Name the blood parasite species.
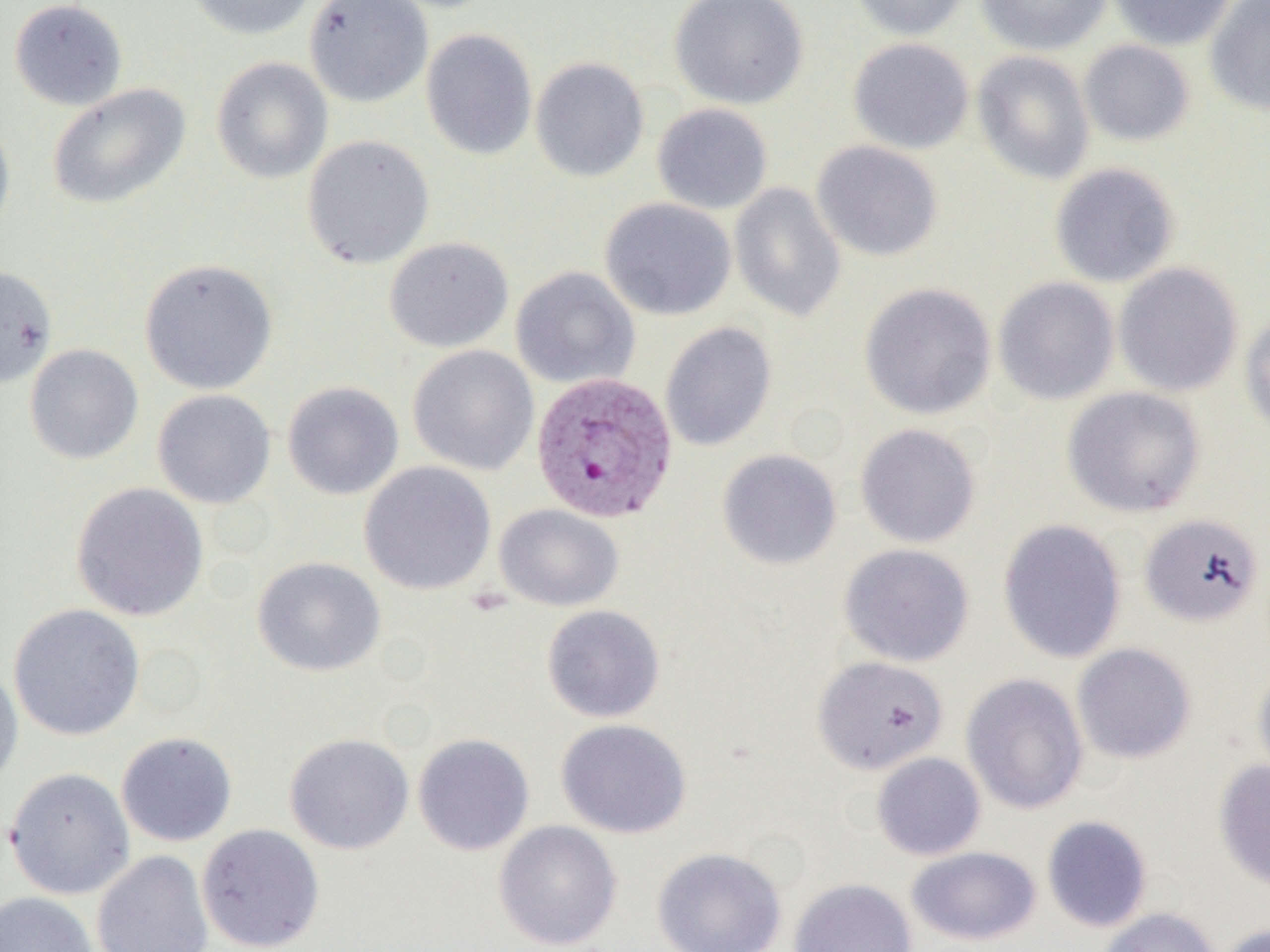

Plasmodium vivax.

Approximate bounding boxes as (x1,y1)-(x2,y2) corner pairs in pixels. Plasmodium vivax-infected red blood cell locations: (529,373)-(676,525). Uninfected red blood cell locations: (8,0)-(128,111), (185,0)-(317,40), (304,0)-(434,107), (669,0)-(810,109), (845,0)-(972,41), (974,0)-(1113,56), (1106,0)-(1239,50), (1205,1)-(1270,116), (421,28)-(538,160), (848,38)-(975,155), (1078,39)-(1195,147), (971,50)-(1095,185), (211,56)-(333,184), (530,57)-(650,182), (47,82)-(191,210), (652,103)-(773,215), (0,114)-(16,246), (301,135)-(435,269), (811,140)-(943,262), (1049,162)-(1180,288), (729,182)-(847,323), (600,197)-(737,320), (383,237)-(514,353), (139,258)-(278,395), (1113,262)-(1243,397), (0,263)-(58,389), (511,267)-(640,389), (993,277)-(1119,405), (859,282)-(997,420), (1239,311)-(1270,437), (660,321)-(777,451), (24,343)-(144,465), (407,344)-(539,475), (282,380)-(404,500), (1062,386)-(1206,518), (152,389)-(276,509), (855,423)-(981,548), (717,448)-(842,570), (359,461)-(496,596), (70,482)-(209,622), (494,503)-(624,611), (1139,513)-(1264,627), (998,519)-(1126,664), (838,543)-(974,667), (252,556)-(386,677), (7,603)-(145,741), (541,604)-(665,723), (1071,643)-(1196,764), (812,656)-(948,775), (0,661)-(24,790), (1252,662)-(1270,789), (961,672)-(1089,814), (556,718)-(691,839), (116,731)-(238,847), (284,732)-(414,855), (412,733)-(535,856), (871,752)-(986,860), (1213,759)-(1270,891), (4,767)-(135,899), (1041,815)-(1152,932), (493,820)-(622,950), (196,824)-(325,952), (906,846)-(1041,945), (652,847)-(786,952), (92,849)-(214,952), (788,878)-(917,952), (0,891)-(98,952), (1097,906)-(1222,952), (1217,923)-(1270,952). Image is 1270×952 pixels. Optical microscopy. 1000x magnification. Single field of view. Thin blood smear.